Comment on the morphology of the erythrocytes.
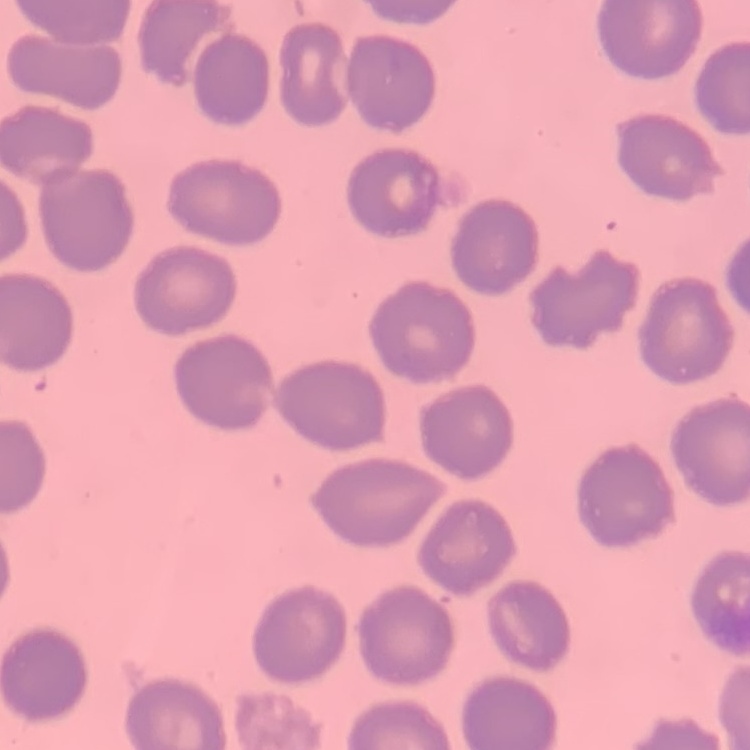
They show no rouleaux formation.

image_type: one tile cut from a larger photomicrograph
preparation: thin blood film
stain: Field's or Giemsa